Identify the parasite.
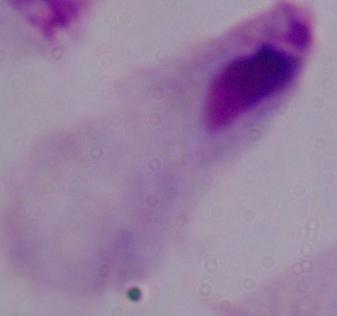

This is a trichomonad.

modality = micrograph
magnification = 1000x